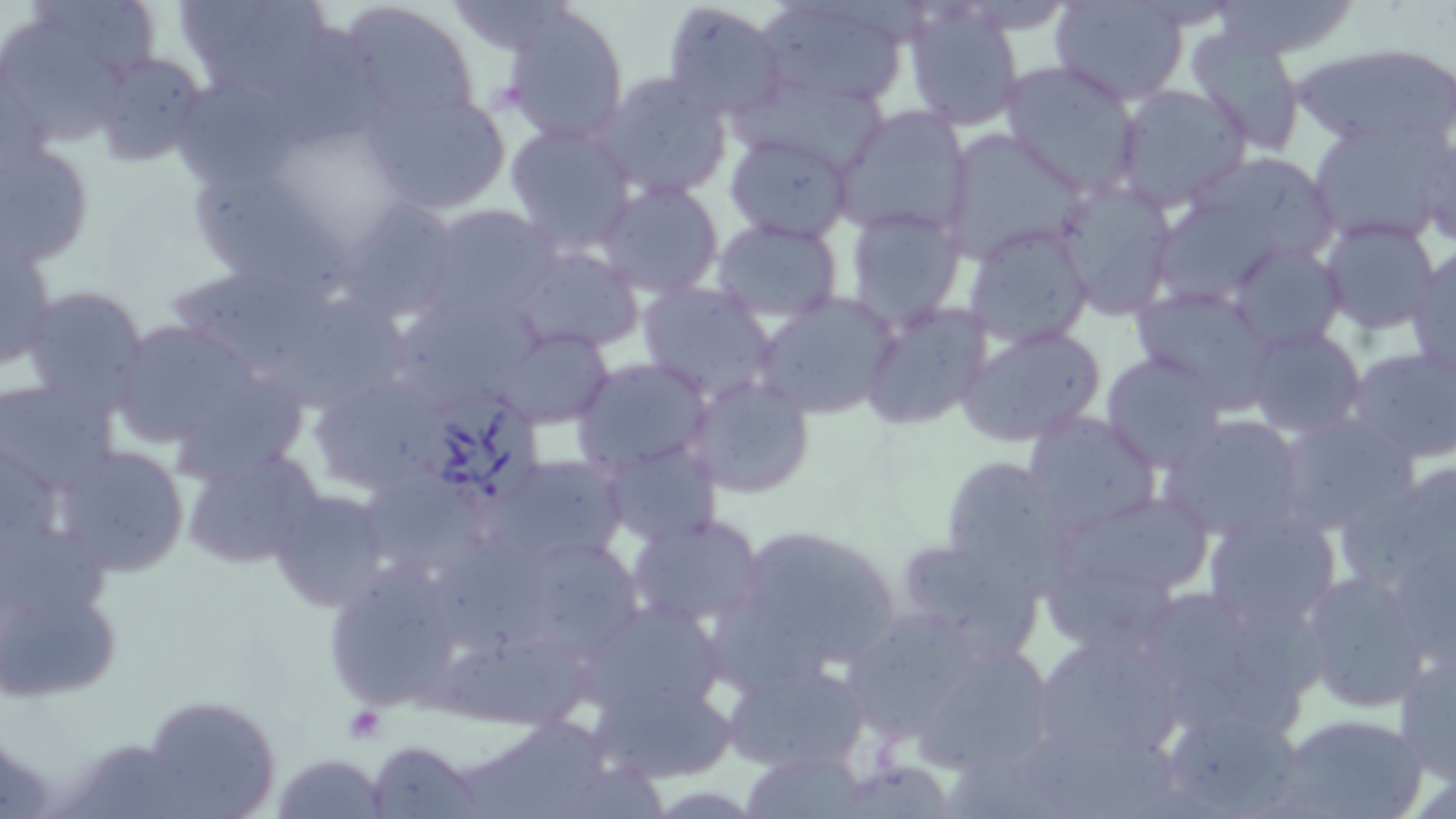

Summary:
  - Coordinate format: approximate bounding boxes as (x1, y1, x2, y2) in pixels
  - Uninfected red blood cell locations: (171, 0, 335, 100), (336, 0, 483, 130), (755, 0, 912, 108), (1051, 0, 1189, 104), (1209, 0, 1362, 60), (661, 1, 789, 123), (446, 2, 570, 55), (1, 3, 147, 143), (500, 3, 630, 143), (902, 5, 1026, 131), (275, 25, 395, 153), (1185, 29, 1306, 154), (1291, 42, 1456, 154), (86, 51, 212, 168), (998, 59, 1145, 197), (590, 70, 735, 200), (741, 71, 889, 177), (181, 82, 300, 193), (1110, 84, 1253, 213), (360, 86, 511, 215), (834, 107, 973, 240), (1302, 119, 1449, 244), (1417, 120, 1455, 249), (505, 124, 636, 254), (942, 130, 1083, 257), (724, 132, 854, 243), (1, 140, 95, 268), (1189, 155, 1337, 251), (197, 173, 355, 301), (1052, 176, 1180, 320), (593, 179, 724, 299), (338, 198, 459, 322), (415, 203, 562, 327), (1158, 203, 1277, 299), (844, 207, 966, 331), (1318, 217, 1441, 335), (712, 218, 843, 324), (963, 223, 1094, 350), (0, 237, 54, 376), (1223, 240, 1348, 352), (508, 244, 644, 354), (1407, 245, 1456, 378), (805, 247, 964, 383), (171, 267, 339, 363), (636, 280, 779, 403), (1130, 284, 1281, 411), (19, 288, 150, 413), (754, 292, 900, 421), (267, 297, 417, 408), (860, 297, 993, 431), (103, 315, 282, 458), (956, 322, 1107, 448), (1243, 326, 1365, 438), (499, 327, 614, 428), (1344, 344, 1456, 464), (1100, 352, 1225, 472), (570, 357, 714, 477), (686, 374, 817, 499), (317, 376, 450, 486), (2, 380, 117, 494), (1023, 410, 1164, 537), (1274, 410, 1416, 535), (1161, 414, 1311, 540), (602, 440, 722, 548), (51, 443, 190, 576), (177, 444, 323, 572), (486, 452, 630, 566), (941, 456, 1072, 592), (1339, 460, 1456, 604), (370, 474, 495, 569), (266, 488, 395, 613), (1052, 489, 1217, 602), (1201, 506, 1343, 632), (626, 511, 769, 631), (0, 528, 114, 619), (749, 529, 898, 655), (528, 534, 636, 655), (890, 534, 1042, 658), (439, 536, 550, 653), (319, 555, 470, 714), (1298, 568, 1438, 711), (1045, 569, 1188, 645), (1128, 581, 1322, 744), (706, 594, 839, 700), (1, 599, 117, 702), (572, 599, 728, 720), (848, 609, 976, 748), (1028, 631, 1190, 768), (415, 638, 597, 728), (1393, 646, 1455, 781), (921, 647, 1048, 768), (721, 659, 872, 774), (595, 677, 741, 784), (135, 694, 281, 819), (1157, 703, 1305, 818), (1269, 711, 1429, 819), (459, 719, 617, 818), (1028, 726, 1185, 819), (368, 739, 484, 818), (739, 747, 872, 818), (271, 751, 390, 819), (945, 761, 1067, 819)
  - Babesia divergens-infected red blood cell locations: (424, 390, 541, 506)
  - Slide-level diagnosis: Babesia divergens
  - Preparation: thin blood film
  - Magnification: 1000x
  - Stain: May-Grünwald-Giemsa
  - Image size: 1456×819 pixels
  - Field of view: single
  - Modality: optical microscopy